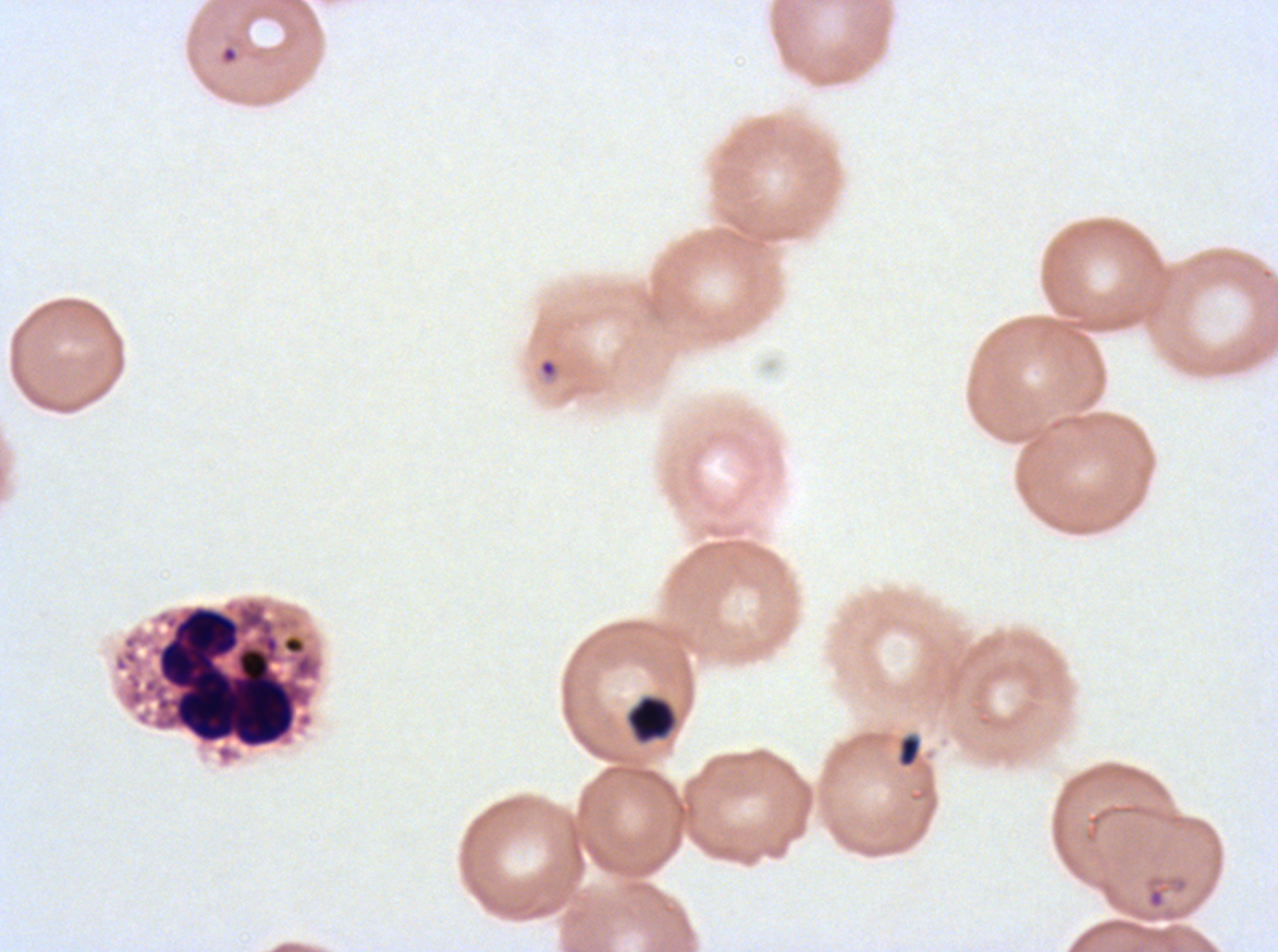
Approximate bounding rectangles given as corner coordinates in pixels from the top-left. Debris locations: (x1=626, y1=694, x2=677, y2=744), (x1=897, y1=733, x2=922, y2=768). Leukocyte locations: (x1=112, y1=595, x2=325, y2=767). Ring locations: (x1=221, y1=45, x2=238, y2=63), (x1=539, y1=359, x2=557, y2=377), (x1=1146, y1=885, x2=1166, y2=910). Thin blood smear. Giemsa-stained preparation. A sub-image separated from a larger composite. P. falciparum cultured ex vivo for 24 to 48 hours, from a patient in The Gambia. Image is 1278×952 pixels.